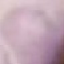

Result: negative for malaria parasites. Giemsa-stained preparation. Thin blood film. Automatically extracted cell patch, resized to 64 × 64 pixels. Acquired by smartphone through the microscope eyepiece.